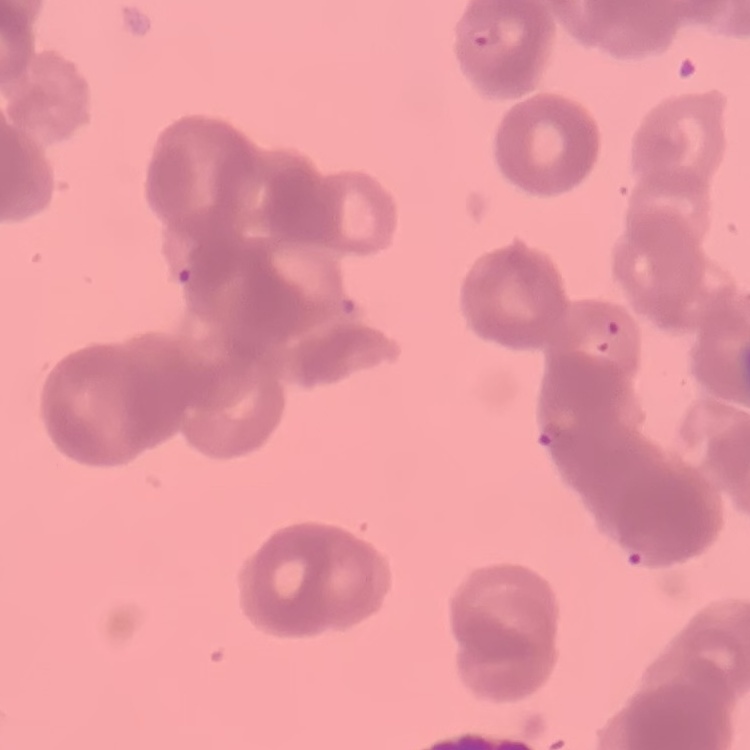
Summary:
  - Erythrocyte morphology: rouleaux formation
  - Stain: Field's or Giemsa
  - Preparation: thin peripheral smear
  - Image type: one tile cut from a larger photomicrograph